Locate and identify every blood parasite.
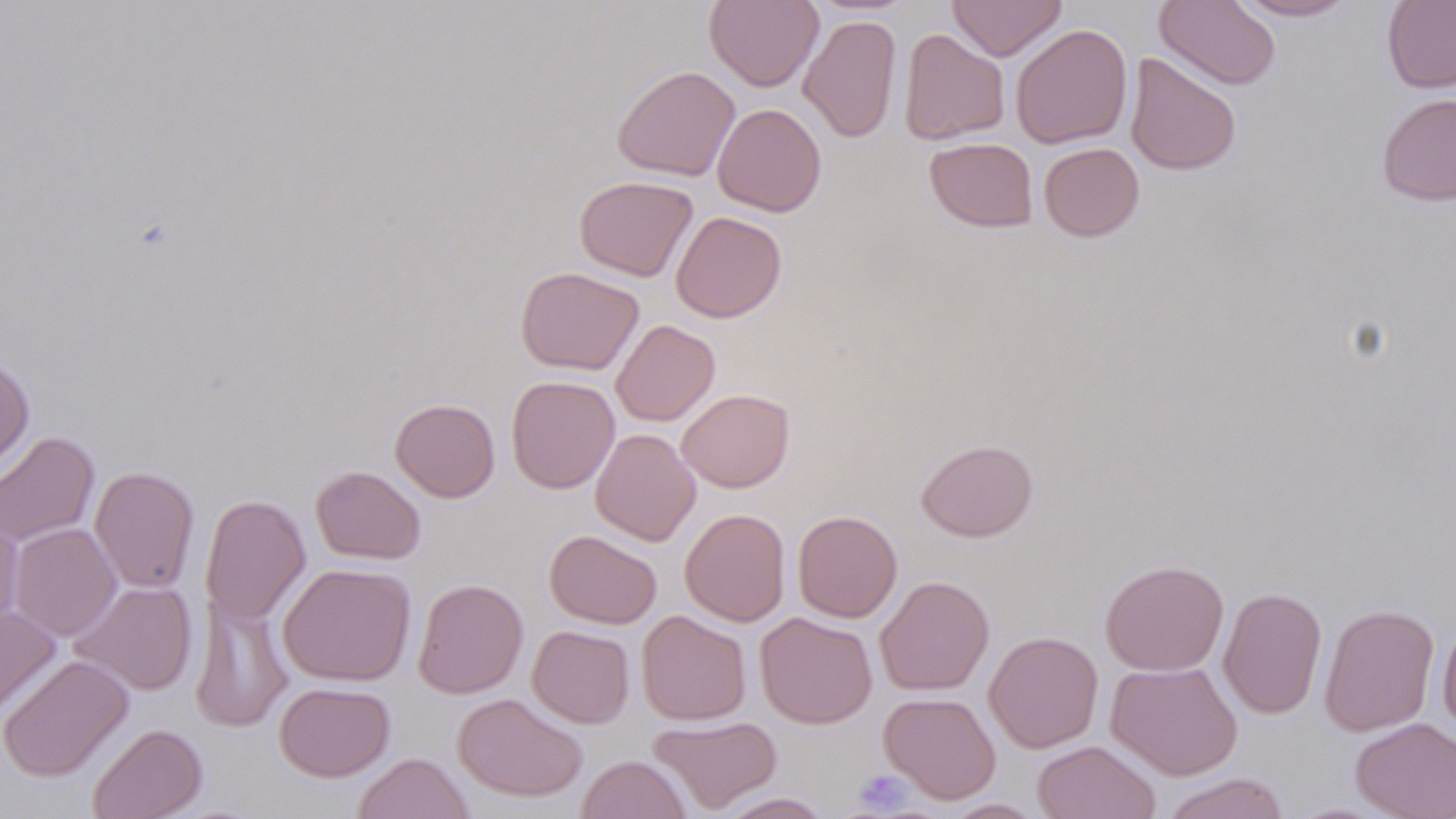
No blood parasites observed.

{
  "slide_level_diagnosis": "no evidence of blood parasites",
  "image_size": "1456×819 pixels",
  "stain": "May-Grünwald-Giemsa",
  "uninfected_red_blood_cell_locations": "approximate bounding boxes as [x1, y1, x2, y2] in pixels: [704, 0, 823, 92], [947, 0, 1066, 61], [1154, 0, 1281, 91], [1233, 0, 1357, 21], [1381, 0, 1456, 94], [798, 13, 902, 143], [1010, 23, 1132, 149], [898, 28, 1010, 145], [1124, 52, 1241, 176], [612, 65, 740, 181], [1376, 93, 1456, 206], [712, 103, 827, 217], [924, 137, 1038, 232], [1038, 142, 1145, 242], [574, 175, 698, 281], [670, 211, 787, 323], [515, 267, 644, 376], [611, 320, 720, 426], [0, 353, 35, 476], [506, 376, 621, 494], [677, 388, 794, 492], [390, 398, 500, 502], [590, 428, 700, 545], [0, 431, 99, 548], [916, 439, 1038, 542], [311, 465, 426, 565], [89, 466, 199, 593], [201, 494, 311, 627], [679, 508, 791, 626], [792, 509, 903, 623], [0, 512, 24, 632], [8, 522, 122, 642], [545, 529, 662, 629], [1100, 559, 1229, 676], [278, 562, 416, 686], [874, 576, 994, 696], [412, 578, 528, 698], [70, 581, 198, 696], [1218, 587, 1327, 719], [190, 593, 292, 733], [1318, 603, 1439, 737], [0, 605, 61, 719], [636, 610, 751, 725], [755, 611, 877, 729], [1437, 616, 1456, 739], [527, 625, 635, 728], [984, 631, 1104, 753], [0, 654, 134, 782], [1105, 660, 1243, 780], [274, 682, 395, 781], [878, 692, 1002, 804], [452, 693, 589, 802], [648, 716, 783, 815], [1350, 718, 1456, 819], [87, 723, 207, 819], [1032, 741, 1161, 819], [353, 753, 475, 819], [577, 755, 691, 819], [1158, 773, 1290, 819], [714, 792, 835, 818], [941, 798, 1045, 818]",
  "magnification": "1000x",
  "preparation": "thin blood smear",
  "field_of_view": "single",
  "platelet_locations": "approximate bounding boxes as [x1, y1, x2, y2] in pixels: [851, 769, 915, 815]",
  "modality": "optical microscopy"
}